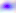
Summary:
  - Magnification: 400x
  - Identification: Toxoplasma gondii
  - Modality: photomicrograph